Outline each Plasmodium ovale-infected red blood cell.
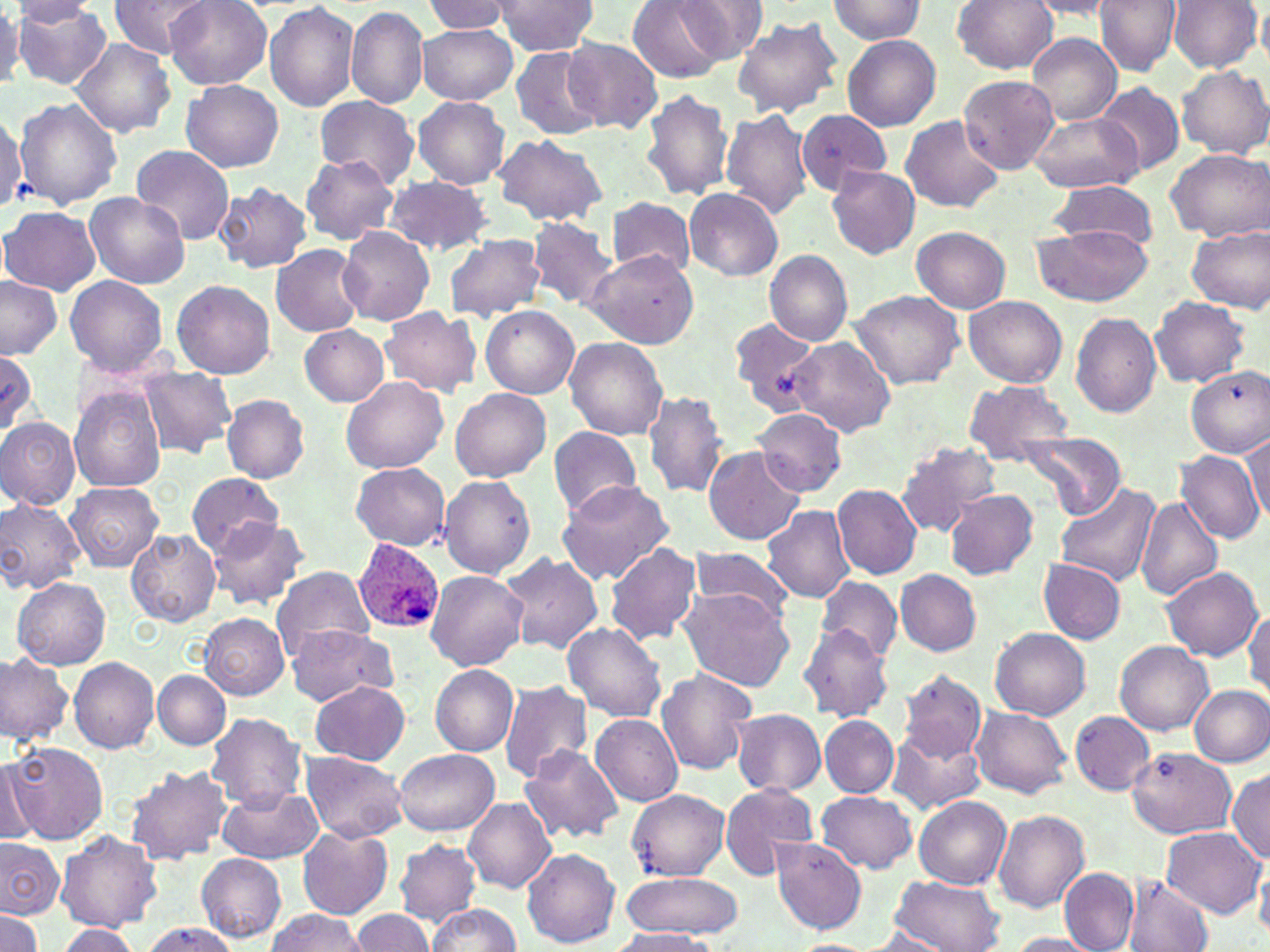

Approximate bounding boxes as (x1, y1, x2, y2) in pixels.
Plasmodium ovale-infected red blood cells: (353, 538, 444, 636).

slide-level diagnosis = Plasmodium ovale
modality = optical microscopy
uninfected red blood cell locations = approximate bounding boxes as (x1, y1, x2, y2) in pixels: (109, 0, 214, 59), (164, 0, 272, 89), (491, 0, 601, 55), (629, 0, 729, 84), (679, 0, 766, 61), (824, 0, 927, 45), (950, 0, 1058, 74), (1096, 0, 1181, 76), (1168, 0, 1260, 72), (12, 1, 100, 27), (421, 1, 511, 36), (1023, 1, 1120, 19), (0, 3, 23, 90), (264, 3, 359, 111), (12, 4, 114, 90), (346, 6, 429, 109), (499, 6, 600, 112), (1257, 6, 1270, 70), (732, 16, 843, 118), (416, 24, 518, 104), (1026, 33, 1120, 124), (842, 35, 941, 132), (563, 37, 663, 133), (71, 38, 175, 138), (510, 47, 604, 139), (1177, 65, 1269, 159), (958, 75, 1058, 174), (180, 80, 284, 173), (1096, 82, 1184, 177), (640, 88, 733, 202), (314, 96, 418, 184), (13, 97, 123, 210), (413, 97, 510, 188), (0, 107, 25, 216), (721, 107, 813, 220), (796, 109, 892, 194), (1027, 111, 1143, 194), (899, 115, 1005, 213), (492, 134, 607, 227), (131, 146, 236, 244), (1164, 146, 1270, 241), (300, 154, 398, 244), (826, 166, 919, 259), (383, 175, 493, 255), (1049, 180, 1159, 250), (213, 183, 312, 274), (683, 187, 784, 282), (84, 193, 191, 289), (607, 197, 695, 277), (1, 206, 101, 294), (527, 216, 618, 311), (1032, 223, 1152, 308), (1189, 224, 1270, 314), (338, 226, 437, 326), (912, 226, 1012, 313), (444, 233, 549, 322), (271, 244, 368, 337), (584, 249, 699, 348), (764, 250, 852, 345), (0, 275, 62, 359), (66, 276, 167, 376), (171, 279, 276, 379), (850, 290, 964, 390), (963, 295, 1066, 387), (1149, 297, 1250, 387), (379, 306, 482, 397), (482, 306, 578, 398), (1069, 312, 1162, 419), (730, 315, 822, 410), (299, 325, 389, 406), (564, 336, 667, 440), (786, 336, 894, 437), (0, 351, 38, 431), (1186, 364, 1270, 455), (138, 366, 235, 457), (342, 375, 448, 473), (963, 380, 1076, 463), (70, 385, 167, 492), (451, 387, 550, 483), (643, 390, 728, 499), (221, 394, 310, 483), (751, 409, 848, 497), (0, 416, 81, 511), (548, 426, 642, 519), (1011, 434, 1127, 517), (1243, 434, 1270, 521), (894, 441, 1002, 536), (704, 447, 802, 546), (1175, 449, 1265, 546), (350, 463, 450, 550), (184, 474, 286, 556), (439, 476, 537, 579), (554, 477, 676, 584), (66, 482, 162, 572), (831, 484, 923, 579), (1055, 487, 1159, 584), (943, 488, 1040, 580), (1134, 495, 1224, 601), (0, 497, 85, 595), (762, 504, 855, 602), (207, 515, 312, 612), (124, 528, 220, 627), (603, 542, 701, 646), (685, 545, 797, 620), (500, 553, 604, 654), (1038, 558, 1127, 643), (1160, 566, 1265, 660), (269, 567, 377, 660), (895, 569, 982, 656), (425, 570, 528, 672), (817, 576, 902, 662), (13, 577, 110, 670), (3, 582, 88, 747), (679, 584, 796, 693), (1246, 606, 1270, 701), (199, 613, 288, 700), (561, 622, 666, 721), (798, 623, 893, 722), (285, 625, 398, 706), (992, 627, 1091, 720), (1115, 641, 1211, 735), (0, 654, 72, 745), (70, 657, 160, 753), (431, 664, 519, 755), (655, 669, 758, 777), (897, 669, 985, 761), (153, 670, 230, 749), (307, 679, 411, 766), (499, 681, 593, 783), (1191, 686, 1270, 766), (970, 706, 1071, 799), (732, 709, 826, 796), (1070, 711, 1154, 795), (205, 713, 308, 809), (590, 715, 684, 807), (820, 715, 899, 798), (888, 730, 985, 815), (9, 742, 107, 843), (518, 745, 625, 845), (1125, 746, 1238, 837), (393, 749, 500, 836), (300, 752, 407, 843), (2, 757, 41, 844), (124, 763, 232, 866), (1229, 768, 1270, 863), (719, 784, 820, 878), (215, 785, 322, 864), (626, 789, 730, 879), (815, 792, 918, 873), (915, 796, 1011, 890), (463, 797, 556, 894), (993, 810, 1091, 913), (298, 825, 393, 919), (1161, 826, 1267, 919), (56, 829, 161, 932), (0, 836, 63, 918), (769, 837, 868, 935), (395, 838, 480, 926), (522, 848, 621, 948), (196, 853, 286, 942), (1255, 857, 1270, 937), (1060, 868, 1138, 951), (622, 872, 741, 938), (891, 875, 1004, 952), (1123, 876, 1214, 952), (425, 903, 522, 952), (267, 910, 369, 951), (348, 910, 434, 952), (0, 911, 42, 950), (136, 922, 239, 952), (52, 927, 143, 952), (864, 928, 947, 951), (607, 929, 717, 951), (1007, 933, 1100, 951), (789, 938, 877, 951)
magnification = 1000x
preparation = thin blood smear
image size = 1270×952 pixels
field of view = single
stain = May-Grünwald-Giemsa